Locate and identify every blood parasite.
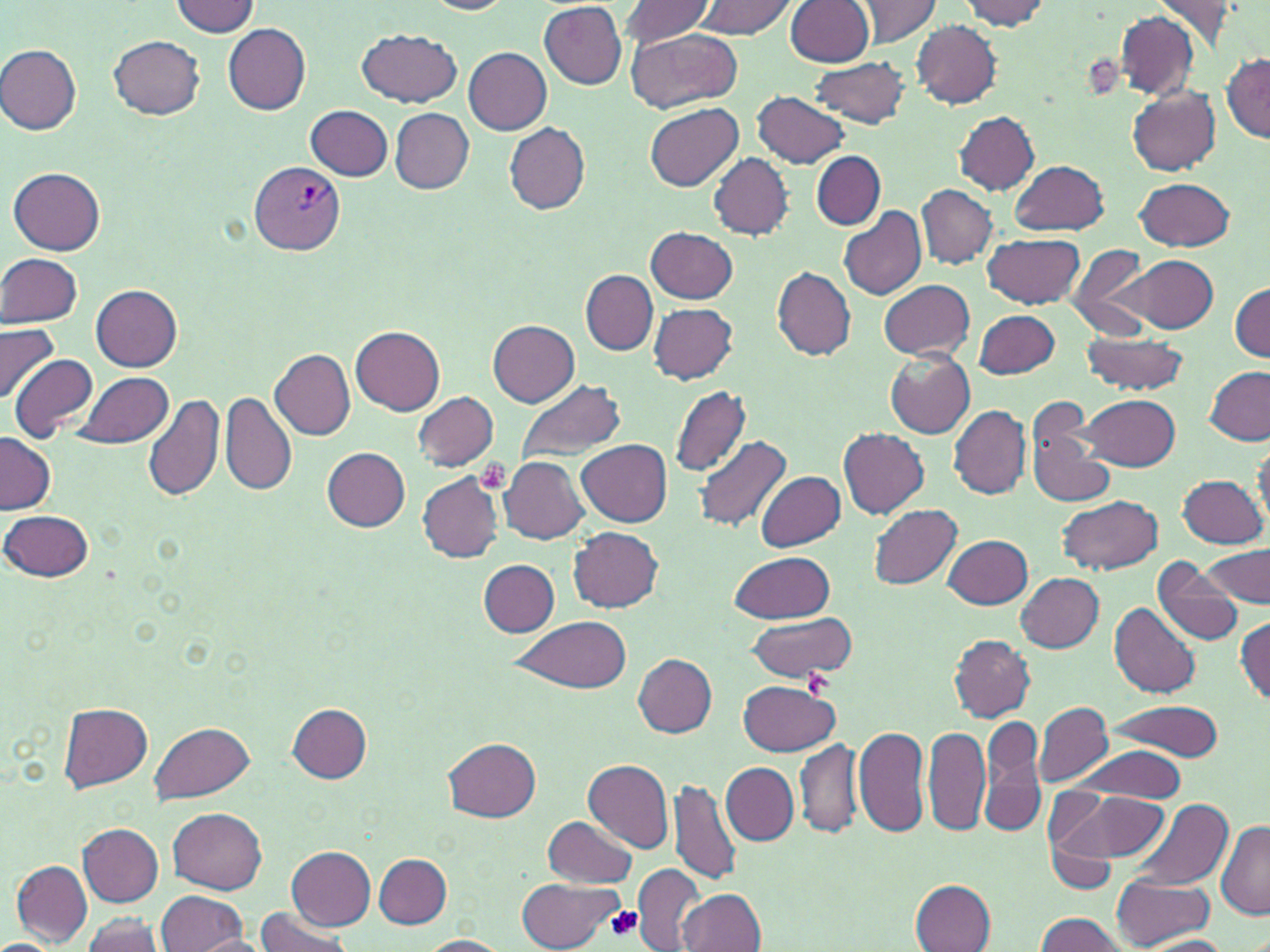

Approximate bounding boxes as (x1, y1, x2, y2) in pixels.
Plasmodium vivax-infected red blood cells: (249, 162, 343, 254).
No Plasmodium falciparum, Plasmodium ovale, Plasmodium malariae, Babesia divergens, or Trypanosoma brucei observed.

{
  "slide_level_diagnosis": "Plasmodium vivax",
  "platelet_locations": "approximate bounding boxes as (x1, y1, x2, y2) in pixels: (1085, 53, 1123, 101), (475, 459, 512, 494), (802, 671, 832, 695), (606, 905, 644, 943)",
  "uninfected_red_blood_cell_locations": "approximate bounding boxes as (x1, y1, x2, y2) in pixels: (621, 0, 716, 47), (695, 0, 795, 39), (786, 0, 873, 67), (851, 0, 942, 46), (960, 0, 1050, 29), (1152, 0, 1239, 49), (170, 1, 260, 37), (422, 1, 515, 15), (539, 2, 626, 89), (1114, 9, 1198, 97), (912, 21, 1002, 107), (222, 22, 312, 114), (358, 28, 463, 107), (627, 28, 742, 114), (109, 35, 205, 119), (1, 44, 82, 134), (463, 47, 551, 134), (1222, 54, 1270, 142), (810, 56, 912, 129), (1128, 88, 1222, 176), (752, 91, 851, 168), (645, 102, 743, 193), (306, 104, 393, 181), (391, 108, 474, 194), (954, 111, 1040, 194), (504, 122, 590, 214), (812, 152, 885, 229), (709, 153, 793, 240), (1010, 160, 1109, 236), (10, 167, 105, 256), (1134, 177, 1236, 252), (917, 185, 997, 267), (838, 207, 927, 300), (647, 227, 737, 302), (983, 232, 1083, 309), (1065, 243, 1155, 338), (1, 252, 83, 328), (1113, 255, 1218, 331), (1072, 259, 1172, 388), (773, 267, 857, 359), (581, 270, 657, 354), (879, 279, 974, 360), (1231, 283, 1269, 360), (91, 284, 182, 371), (647, 303, 737, 384), (974, 310, 1059, 379), (487, 318, 580, 406), (0, 323, 59, 402), (351, 325, 446, 415), (1080, 331, 1187, 395), (270, 347, 356, 439), (886, 351, 975, 439), (9, 353, 98, 442), (1203, 366, 1269, 446), (74, 371, 174, 450), (516, 379, 626, 463), (669, 383, 751, 478), (144, 392, 226, 504), (413, 392, 498, 471), (221, 393, 296, 496), (1081, 393, 1181, 470), (948, 405, 1031, 499), (1025, 415, 1113, 510), (839, 428, 929, 519), (0, 431, 55, 514), (693, 435, 791, 533), (578, 439, 672, 527), (322, 447, 410, 531), (500, 455, 591, 544), (755, 470, 845, 551), (416, 473, 505, 562), (1177, 473, 1266, 548), (1057, 495, 1163, 574), (869, 503, 963, 590), (1, 510, 94, 582), (568, 527, 663, 612), (944, 534, 1034, 609), (1201, 543, 1270, 608), (730, 550, 835, 623), (1152, 558, 1243, 647), (479, 559, 559, 637), (1016, 572, 1103, 651), (1109, 601, 1200, 699), (745, 613, 859, 683), (1235, 616, 1269, 705), (505, 617, 632, 692), (950, 635, 1035, 721), (632, 652, 717, 737), (739, 680, 839, 755), (1104, 700, 1224, 761), (1033, 701, 1113, 787), (59, 702, 154, 792), (287, 702, 370, 782), (981, 715, 1047, 838), (150, 723, 255, 804), (853, 724, 930, 839), (923, 725, 989, 838), (796, 735, 865, 839), (444, 737, 541, 822), (1071, 747, 1187, 802), (585, 759, 675, 851), (721, 762, 798, 844), (669, 776, 742, 886), (1046, 784, 1172, 879), (1127, 798, 1233, 893), (168, 807, 267, 894), (544, 814, 638, 888), (1216, 818, 1270, 919), (78, 823, 163, 905), (286, 847, 375, 929), (374, 855, 453, 928), (12, 860, 92, 944), (633, 865, 705, 951), (1112, 875, 1213, 948), (517, 878, 621, 950), (912, 879, 997, 952), (155, 889, 249, 951), (678, 889, 765, 952), (251, 909, 355, 952), (1036, 912, 1133, 952), (78, 913, 165, 951), (191, 934, 273, 952), (420, 935, 510, 952), (1139, 935, 1236, 951)",
  "field_of_view": "one of a larger specimen",
  "image_size": "1270×952 pixels",
  "magnification": "1000x",
  "modality": "light microscopy",
  "stain": "May-Grünwald-Giemsa",
  "preparation": "thin blood smear"
}